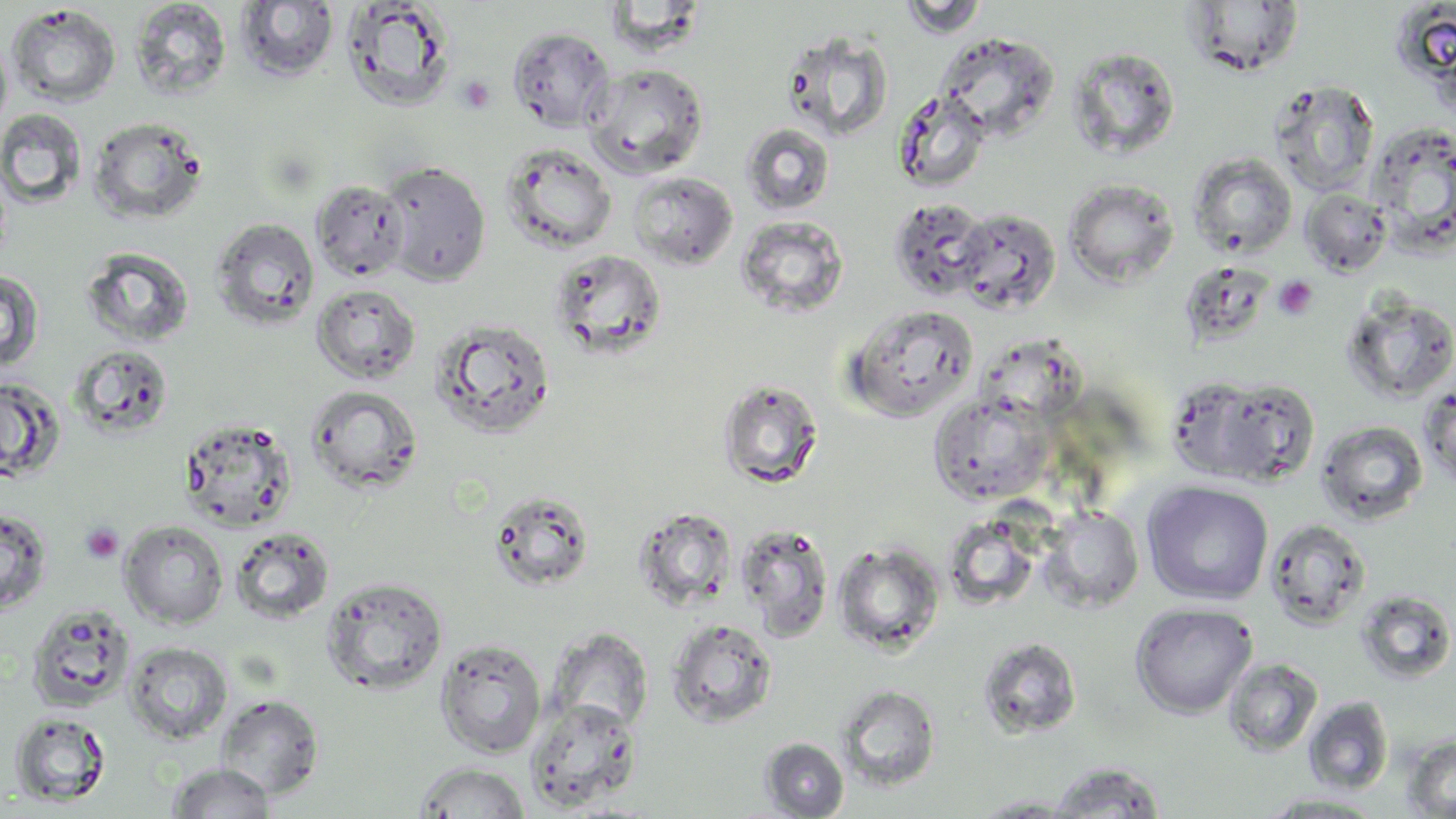

Summary:
  - Coordinate format: approximate bounding boxes as (x1, y1, x2, y2) in pixels
  - Uninfected red blood cell locations: (898, 0, 990, 39), (130, 1, 232, 101), (236, 1, 339, 81), (341, 1, 457, 111), (1182, 2, 1305, 77), (1390, 3, 1456, 92), (6, 4, 121, 107), (508, 27, 615, 133), (781, 30, 894, 142), (933, 31, 1059, 142), (0, 32, 12, 137), (1065, 46, 1181, 161), (585, 63, 709, 178), (1269, 81, 1379, 197), (893, 89, 992, 192), (0, 109, 88, 209), (88, 116, 208, 225), (1367, 121, 1456, 252), (741, 122, 835, 215), (500, 142, 618, 254), (1188, 153, 1297, 258), (380, 160, 492, 287), (628, 171, 738, 270), (1063, 178, 1179, 288), (310, 179, 409, 282), (1300, 188, 1392, 276), (889, 198, 990, 301), (952, 207, 1061, 314), (736, 216, 849, 319), (211, 218, 320, 329), (81, 246, 195, 348), (550, 249, 667, 359), (1178, 266, 1276, 348), (0, 269, 44, 373), (311, 283, 421, 384), (1341, 294, 1456, 404), (845, 306, 978, 422), (431, 317, 556, 439), (971, 337, 1087, 427), (68, 344, 174, 439), (1164, 376, 1267, 480), (0, 377, 65, 483), (717, 377, 824, 489), (1209, 379, 1321, 487), (1419, 384, 1456, 489), (305, 385, 424, 495), (928, 394, 1052, 506), (179, 416, 298, 532), (1315, 420, 1429, 525), (1142, 481, 1274, 606), (488, 490, 595, 592), (633, 507, 737, 611), (1039, 507, 1143, 611), (0, 508, 51, 615), (1264, 518, 1371, 628), (119, 521, 229, 629), (736, 524, 835, 642), (230, 527, 335, 624), (832, 542, 944, 656), (321, 576, 448, 695), (1356, 589, 1455, 684), (26, 603, 136, 714), (1130, 603, 1257, 719), (665, 618, 778, 728), (547, 627, 654, 736), (435, 637, 547, 758), (977, 637, 1082, 739), (123, 641, 233, 745), (1223, 658, 1322, 756), (836, 685, 941, 792), (214, 694, 325, 800), (1304, 696, 1394, 795), (525, 698, 643, 812), (9, 711, 112, 807), (1402, 735, 1456, 818), (760, 738, 849, 818), (414, 761, 531, 818), (1044, 761, 1168, 818), (166, 763, 275, 819), (1253, 793, 1390, 817), (969, 794, 1089, 817)
  - Platelet locations: (457, 75, 496, 114), (1274, 275, 1318, 320), (80, 523, 123, 564)
  - Slide-level diagnosis: no evidence of blood parasites
  - Magnification: 1000x
  - Image size: 1456×819 pixels
  - Modality: light microscopy
  - Stain: May-Grünwald-Giemsa
  - Field of view: single
  - Preparation: thin blood film